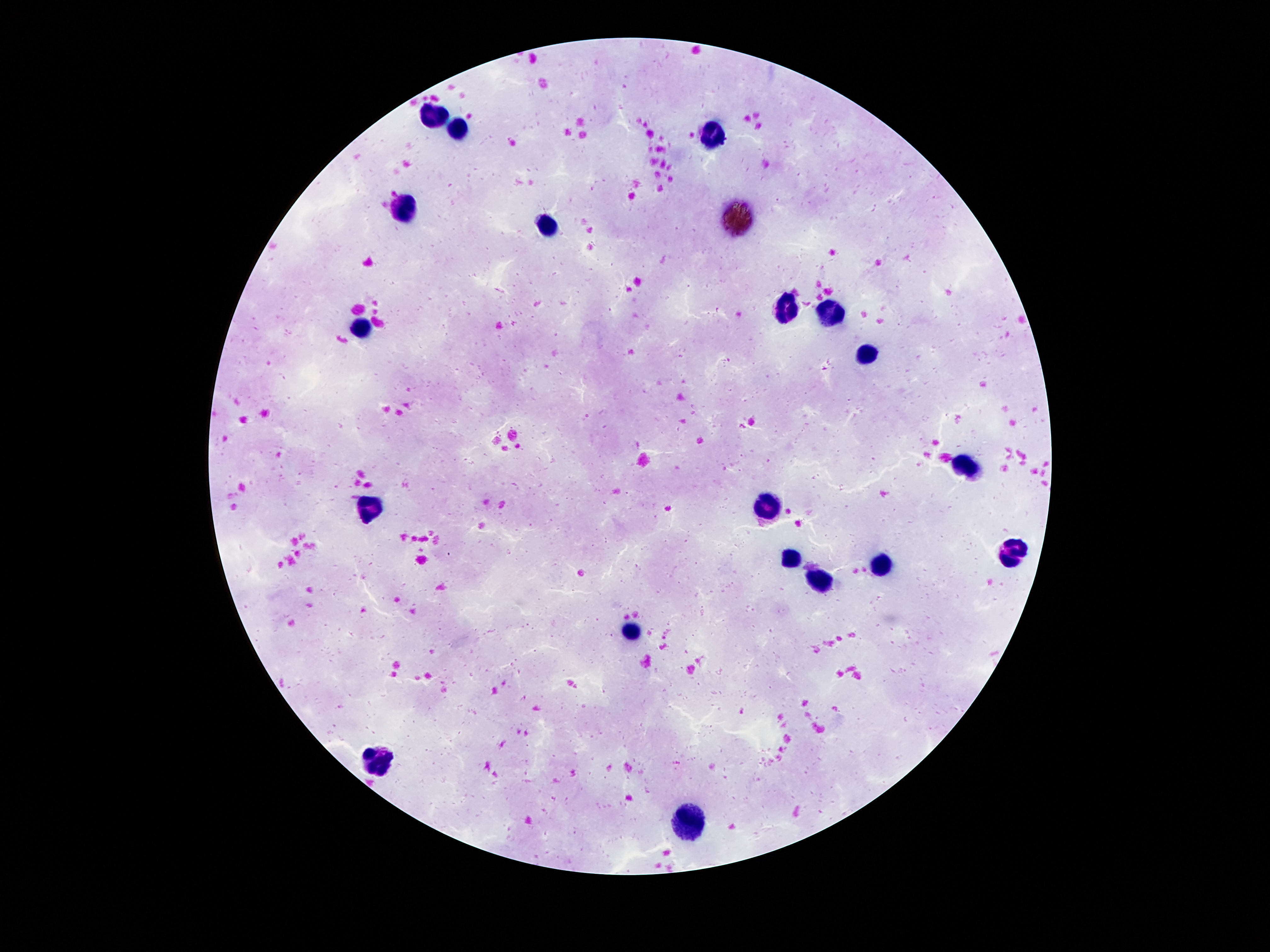 Approximate centers as {x, y} in pixels. Leukocyte locations: {437, 113}, {458, 128}, {714, 134}, {403, 208}, {548, 227}, {788, 307}, {828, 313}, {359, 331}, {863, 355}, {968, 467}, {769, 506}, {368, 509}, {1012, 549}, {788, 559}, {882, 561}, {821, 580}, {632, 630}, {382, 762}, {693, 828}. 100x magnification. Thick blood film. Smartphone photograph taken through the microscope eyepiece. Giemsa stain. Patient malaria status: uninfected. Single field of view. Image is 1270×952 pixels.